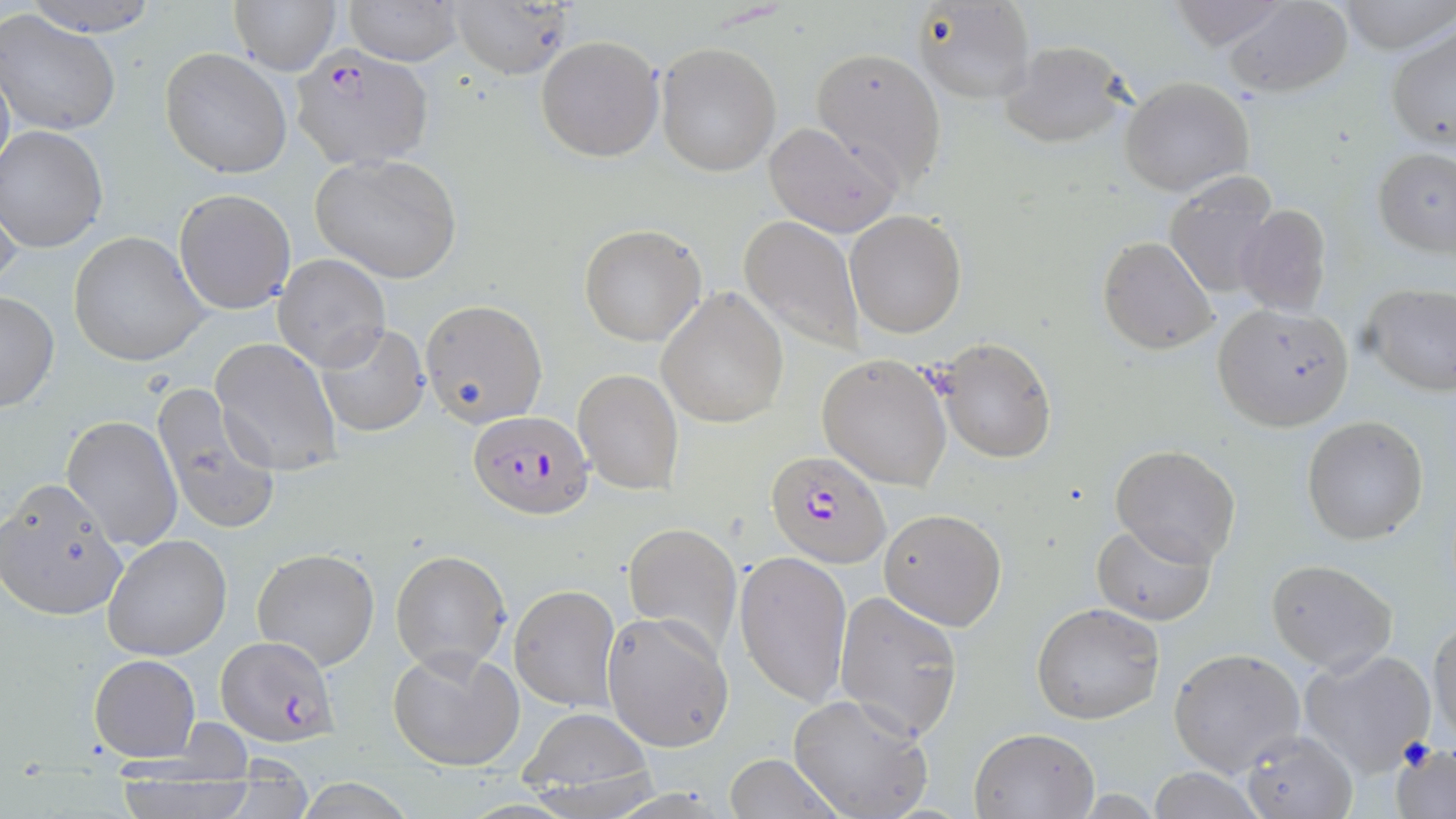

Plasmodium falciparum-infected red blood cell locations = approximate bounding boxes as [x1, y1, x2, y2] in pixels: [286, 47, 434, 170], [466, 410, 592, 518], [766, 448, 889, 567], [217, 636, 339, 747]
slide-level diagnosis = Plasmodium falciparum
modality = light microscopy
field of view = one of a larger specimen
uninfected red blood cell locations = approximate bounding boxes as [x1, y1, x2, y2] in pixels: [14, 0, 165, 40], [227, 0, 339, 74], [343, 0, 464, 66], [449, 0, 575, 80], [911, 0, 1032, 103], [1166, 0, 1293, 50], [1338, 0, 1456, 53], [1223, 2, 1353, 96], [0, 10, 122, 138], [1386, 25, 1455, 152], [537, 36, 664, 161], [998, 39, 1130, 150], [655, 41, 780, 176], [160, 47, 293, 178], [810, 47, 947, 189], [1120, 76, 1254, 197], [763, 120, 902, 237], [1, 127, 109, 252], [1372, 145, 1456, 256], [310, 154, 463, 285], [1162, 171, 1283, 299], [0, 188, 25, 297], [173, 188, 296, 315], [1233, 203, 1333, 317], [844, 210, 966, 338], [738, 214, 865, 355], [577, 224, 707, 346], [68, 230, 210, 369], [1098, 237, 1217, 354], [274, 254, 391, 373], [1361, 284, 1456, 396], [656, 288, 788, 429], [0, 290, 59, 413], [419, 299, 549, 427], [1212, 301, 1356, 431], [314, 322, 430, 437], [211, 337, 342, 476], [928, 337, 1057, 463], [816, 354, 953, 489], [571, 369, 683, 495], [153, 386, 280, 536], [60, 414, 183, 553], [1300, 415, 1430, 544], [1110, 445, 1241, 565], [1, 478, 131, 621], [878, 507, 1007, 630], [1091, 521, 1216, 624], [622, 522, 743, 658], [102, 533, 234, 662], [251, 547, 380, 671], [389, 549, 511, 673], [735, 550, 853, 709], [1265, 559, 1398, 675], [509, 583, 621, 712], [833, 589, 965, 742], [1031, 603, 1165, 725], [603, 612, 733, 751], [1429, 615, 1455, 744], [1300, 645, 1436, 774], [388, 646, 526, 771], [1168, 646, 1306, 777], [89, 653, 200, 761], [788, 693, 934, 819], [518, 711, 654, 799], [969, 728, 1099, 817], [1239, 728, 1355, 819], [1390, 740, 1455, 817], [726, 753, 840, 818], [1146, 767, 1266, 819], [112, 768, 261, 819]
image size = 1456×819 pixels
stain = May-Grünwald-Giemsa
preparation = thin blood smear
magnification = 1000x